Point out every malaria parasite.
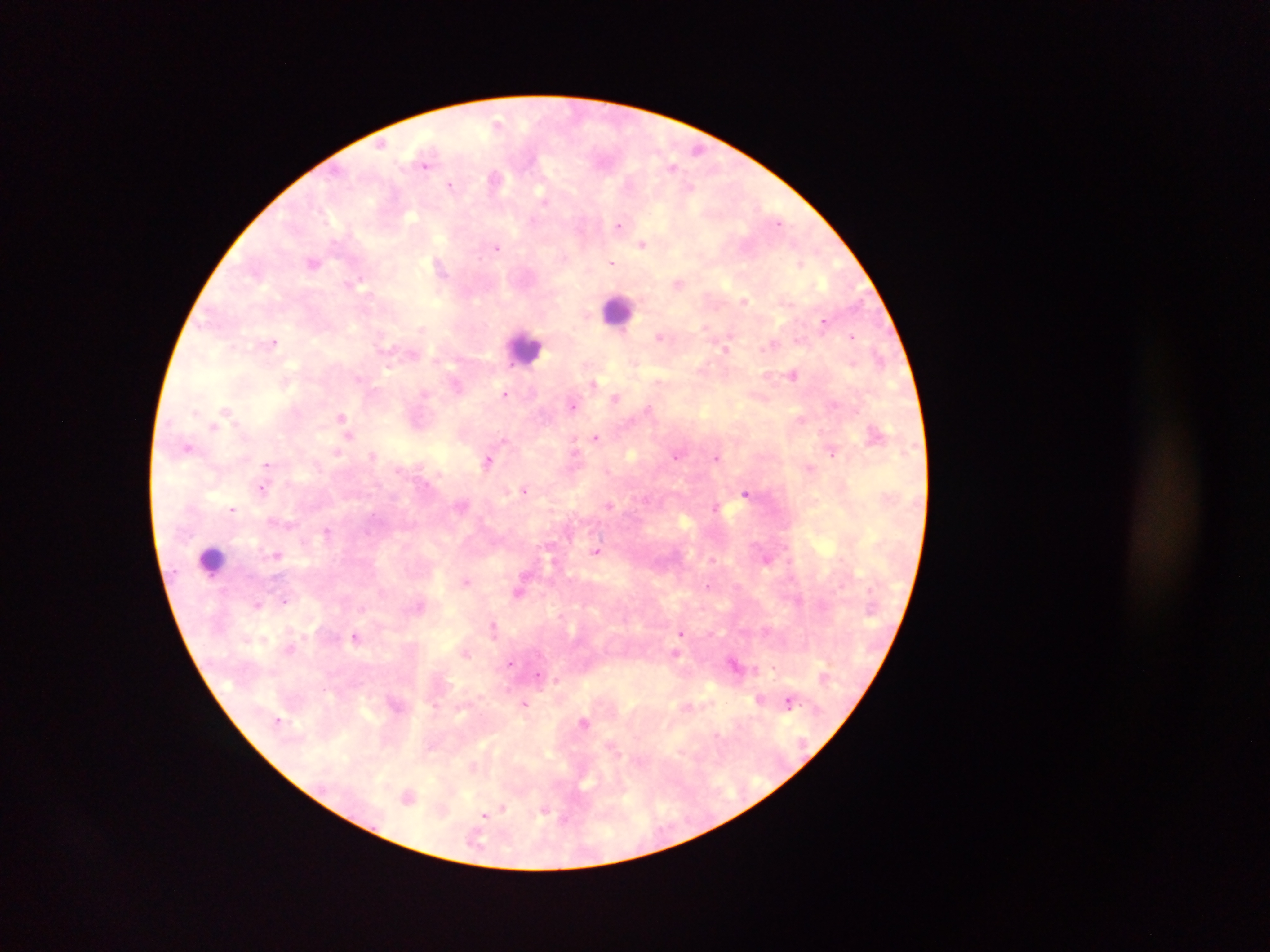
Approximate centers as x y in pixels.
Malaria parasites: 498 123; 382 143; 698 149; 425 163; 673 167; 495 179; 451 185; 690 188; 544 200; 533 221; 779 222; 618 225; 642 243; 498 248; 313 262; 612 262; 800 263; 439 266; 358 282; 678 282; 744 301; 823 321; 706 327; 659 337; 852 337; 274 342; 725 348; 879 356; 793 375; 358 379; 657 381; 594 383; 505 394; 616 397; 573 405; 649 408; 226 409; 196 413; 341 416; 801 419; 214 427; 349 436; 596 437; 187 447; 574 450; 337 452; 832 454; 373 455; 676 457; 716 458; 488 460; 267 464; 809 468; 261 488; 525 490; 746 493; 610 506; 715 507; 233 509; 327 531; 596 552; 276 555; 713 560; 467 580; 707 586; 518 591; 284 601; 256 605; 419 606; 493 625; 681 633; 356 637; 466 653; 676 653; 510 663; 734 664; 538 676; 556 679; 759 699; 788 702; 525 704; 584 722; 716 734; 408 797; 503 808; 544 812; 484 814.

Summary:
  - Leukocyte locations: 618 310; 524 348; 212 560
  - Field of view: single
  - Country: Ghana
  - Preparation: thick blood smear
  - Capture: mobile-phone photograph through a microscope
  - Image size: 1270×952 pixels